Comment on the morphology of the red blood cells.
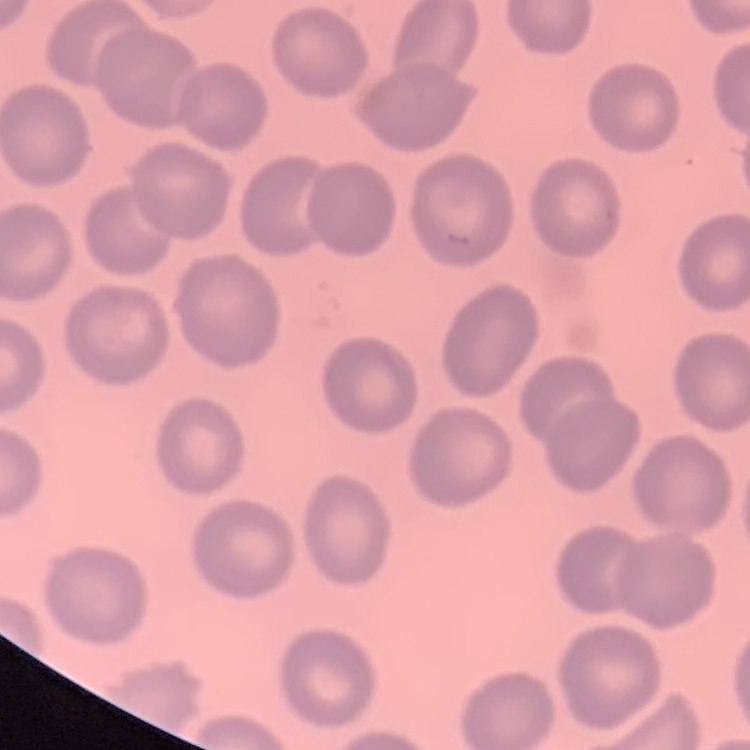
No rouleaux formation.

preparation: thin peripheral smear
image_type: one tile cut from a larger photomicrograph
stain: Field's or Giemsa